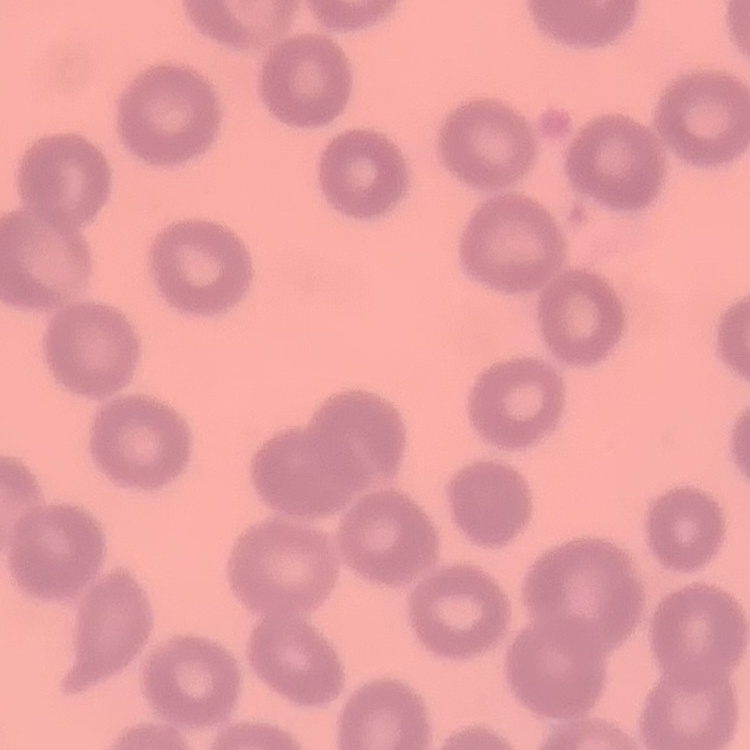 The red blood cells exhibit no rouleaux formation. Thin peripheral smear. One tile cut from a larger photomicrograph. Stained with either Field's or Giemsa.